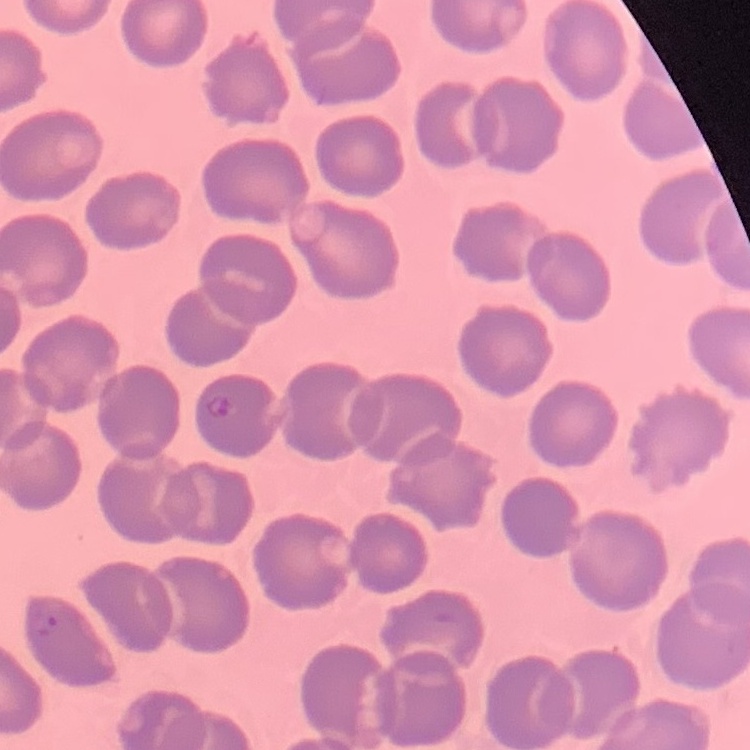

Summary:
  - Erythrocyte morphology: no rouleaux formation
  - Preparation: thin peripheral smear
  - Image type: one tile cut from a larger photomicrograph
  - Stain: Field's or Giemsa